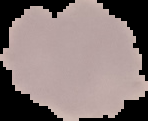
preparation = thin blood smear
image size = 148×121 pixels
malaria status = uninfected
image type = segmented cell region on a black background